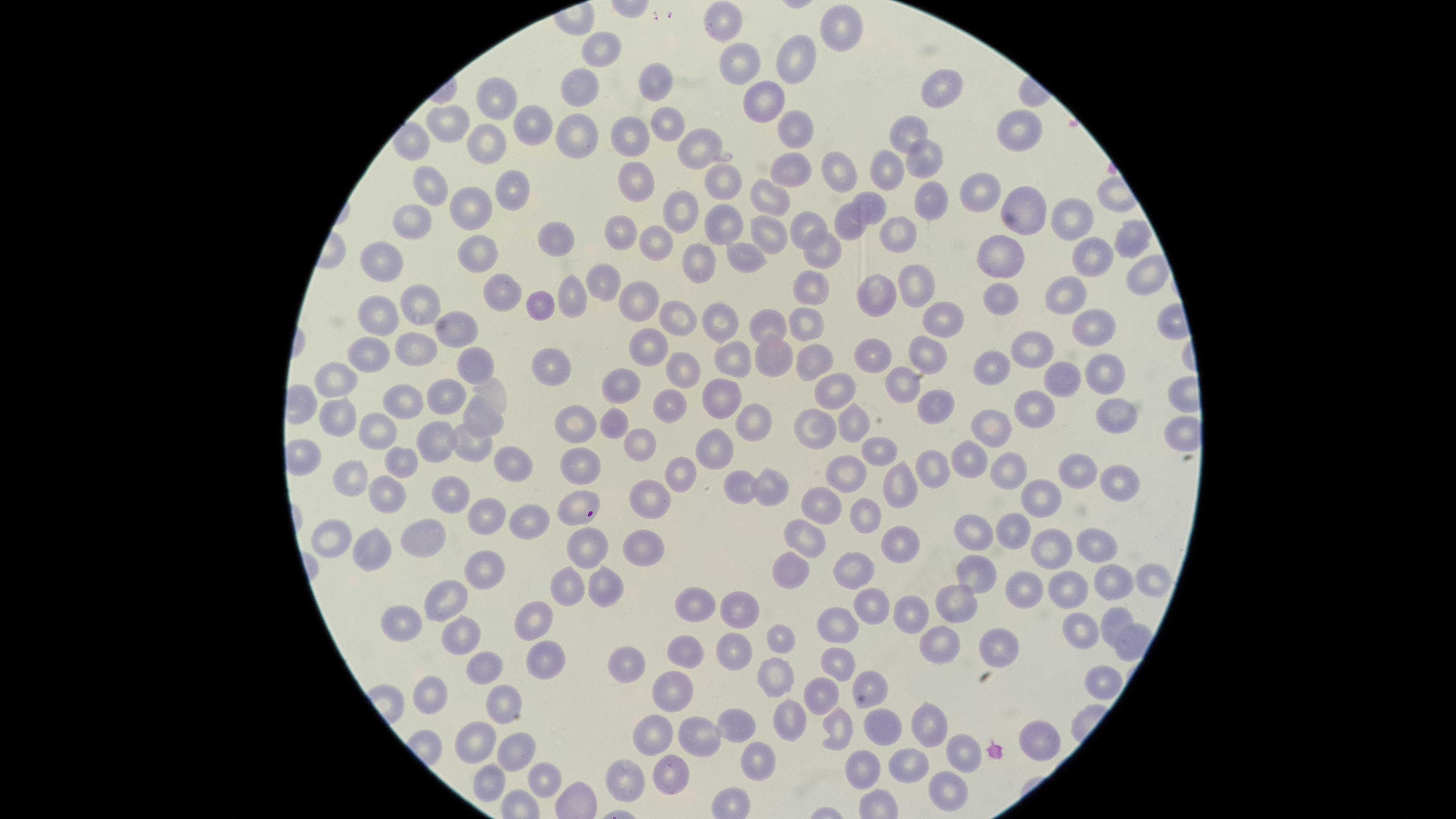
{
  "visible_region": "circular",
  "preparation": "thin smear of blood",
  "stain": "Giemsa",
  "presence": "no malaria parasites identified",
  "uninfected_red_blood_cells": "approximate marker points as (x, y) in pixels: (729, 20), (839, 27), (605, 46), (795, 61), (743, 73), (652, 78), (584, 87), (935, 88), (492, 95), (762, 105), (448, 122), (533, 123), (664, 128), (791, 133), (1018, 134), (910, 136), (629, 137), (571, 138), (490, 147), (700, 147), (919, 162), (791, 169), (879, 169), (836, 170), (430, 177), (718, 185), (637, 186), (509, 189), (971, 196), (771, 201), (927, 202), (474, 210), (668, 210), (871, 210), (1017, 216), (1060, 218), (805, 224), (845, 225), (408, 226), (722, 226), (620, 231), (770, 233), (556, 235), (1122, 235), (895, 236), (653, 246), (480, 249), (815, 253), (1003, 253), (744, 254), (1084, 260), (378, 262), (703, 267), (914, 278), (1143, 279), (605, 281), (811, 286), (496, 294), (872, 294), (1062, 296), (1006, 297), (567, 299), (637, 301), (416, 304), (536, 304), (679, 316), (933, 318), (376, 319), (715, 321), (1086, 322), (808, 325), (765, 327), (455, 329), (648, 347), (363, 351), (1028, 351), (920, 354), (865, 356), (412, 358), (728, 358), (473, 361), (803, 362), (682, 365), (770, 365), (550, 367), (995, 367), (1100, 374), (333, 376), (904, 381), (624, 382), (840, 387), (1062, 388), (492, 393), (935, 400), (442, 401), (670, 403), (718, 403), (400, 406), (1035, 407), (336, 410), (747, 418), (483, 420), (578, 421), (619, 421), (851, 421), (1117, 422), (806, 426), (995, 427), (377, 431), (639, 440), (472, 442), (713, 446), (431, 448), (873, 449), (967, 458), (393, 461), (585, 461), (507, 463), (680, 464), (1008, 466), (845, 469), (935, 472), (1082, 473), (897, 475), (350, 480), (1113, 483), (740, 487), (769, 487), (454, 491), (654, 491), (382, 495), (1044, 500), (573, 502), (818, 506), (484, 513), (868, 513), (528, 516), (973, 530), (807, 531), (1007, 531), (427, 533), (327, 534), (897, 541), (1092, 541), (586, 542), (652, 545), (370, 546), (1049, 548), (783, 566), (858, 568), (973, 573), (480, 574), (1145, 576), (602, 582), (1106, 582), (566, 584), (1022, 585), (1068, 585), (445, 592), (951, 602), (692, 603), (870, 607), (905, 608), (737, 612), (405, 613), (1110, 619), (531, 621), (1079, 633), (839, 636), (460, 639), (939, 639), (780, 643), (682, 649), (994, 650), (545, 657), (734, 657), (834, 658), (480, 665), (628, 666), (772, 668), (1098, 678), (868, 687), (426, 688), (826, 690), (671, 692), (501, 697), (786, 716), (883, 724), (837, 725), (927, 726), (734, 727), (649, 733), (699, 736), (1037, 738), (477, 743), (964, 744), (512, 749), (751, 756), (914, 757), (859, 769), (668, 773), (547, 774), (486, 780), (618, 780), (944, 792)",
  "capture": "smartphone photograph through the microscope eyepiece",
  "field_of_view": "single",
  "image_size": "1456×819 pixels"
}